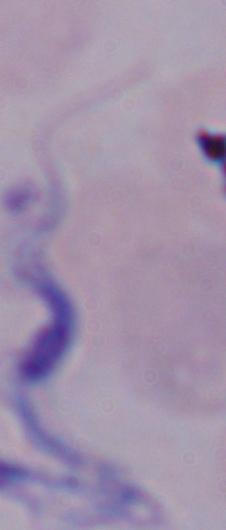
Summary:
  - Identification: trypanosome
  - Magnification: 1000x
  - Modality: micrograph